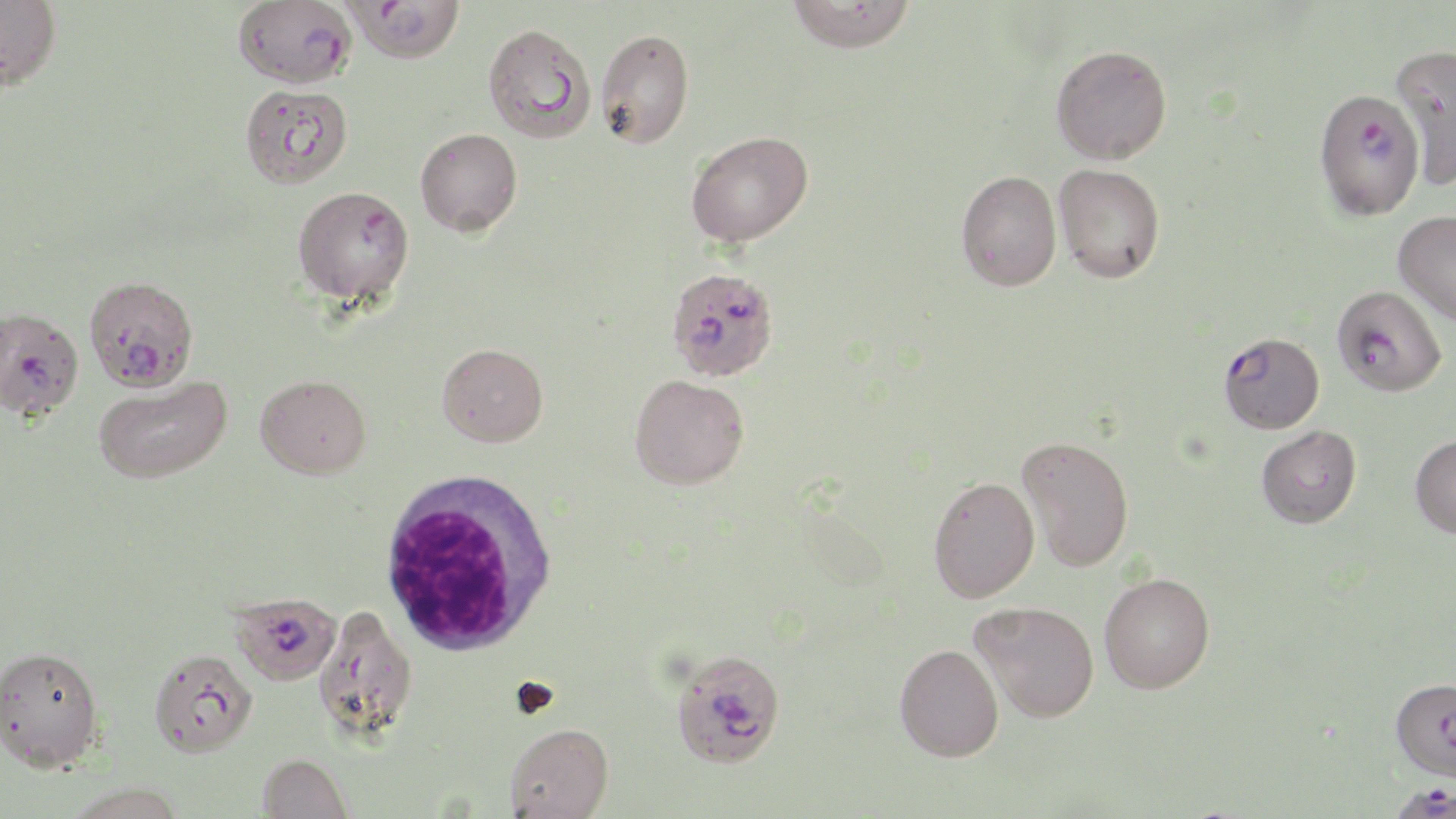

Summary:
  - Coordinate format: approximate bounding boxes as named x1/y1/x2/y2 corners in pixels
  - Uninfected red blood cell locations: (x1=0, y1=0, x2=61, y2=89), (x1=786, y1=0, x2=916, y2=53), (x1=483, y1=23, x2=595, y2=143), (x1=596, y1=28, x2=694, y2=148), (x1=1050, y1=44, x2=1172, y2=164), (x1=1389, y1=44, x2=1456, y2=190), (x1=239, y1=84, x2=353, y2=189), (x1=415, y1=127, x2=523, y2=237), (x1=686, y1=130, x2=813, y2=246), (x1=1054, y1=164, x2=1165, y2=283), (x1=955, y1=170, x2=1061, y2=291), (x1=1393, y1=210, x2=1456, y2=326), (x1=437, y1=343, x2=548, y2=447), (x1=255, y1=374, x2=371, y2=479), (x1=629, y1=374, x2=750, y2=489), (x1=94, y1=375, x2=232, y2=484), (x1=1256, y1=425, x2=1362, y2=528), (x1=1410, y1=435, x2=1456, y2=538), (x1=1017, y1=436, x2=1134, y2=571), (x1=928, y1=475, x2=1040, y2=603), (x1=1100, y1=572, x2=1215, y2=693), (x1=970, y1=600, x2=1099, y2=722), (x1=311, y1=605, x2=417, y2=742), (x1=895, y1=643, x2=1004, y2=761), (x1=0, y1=645, x2=104, y2=772), (x1=148, y1=648, x2=257, y2=757), (x1=1390, y1=678, x2=1456, y2=781), (x1=504, y1=723, x2=614, y2=819), (x1=257, y1=753, x2=353, y2=818), (x1=65, y1=782, x2=187, y2=819)
  - White blood cell locations: (x1=377, y1=469, x2=559, y2=657)
  - Plasmodium falciparum-infected red blood cell locations: (x1=232, y1=0, x2=356, y2=89), (x1=344, y1=1, x2=465, y2=65), (x1=1313, y1=87, x2=1427, y2=220), (x1=292, y1=186, x2=415, y2=306), (x1=672, y1=274, x2=776, y2=383), (x1=83, y1=276, x2=198, y2=393), (x1=1332, y1=285, x2=1447, y2=397), (x1=0, y1=305, x2=84, y2=422), (x1=1218, y1=331, x2=1324, y2=434), (x1=229, y1=591, x2=342, y2=686), (x1=670, y1=648, x2=786, y2=769), (x1=1383, y1=780, x2=1456, y2=818)
  - Slide-level diagnosis: Plasmodium falciparum
  - Stain: May-Grünwald-Giemsa
  - Image size: 1456×819 pixels
  - Modality: optical microscopy
  - Field of view: one of a larger specimen
  - Magnification: 1000x
  - Preparation: thin blood smear